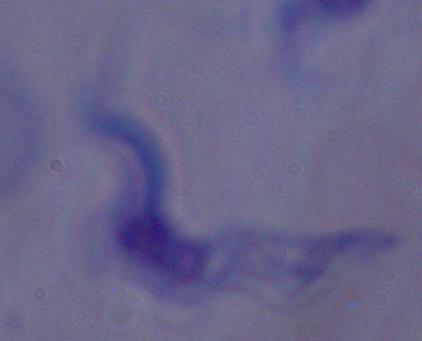
modality = micrograph
magnification = 1000x
identification = trypanosome